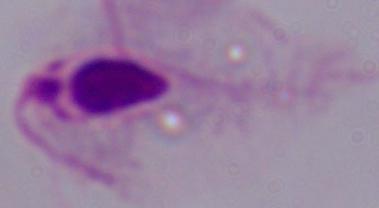
1000x magnification. Micrograph. A trichomonad is shown.